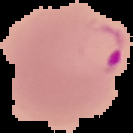

image size = 133×133 pixels
image type = segmented cell region with the area outside set to black
malaria status = parasitized
preparation = thin blood smear